Locate every leukocyte (white blood cell).
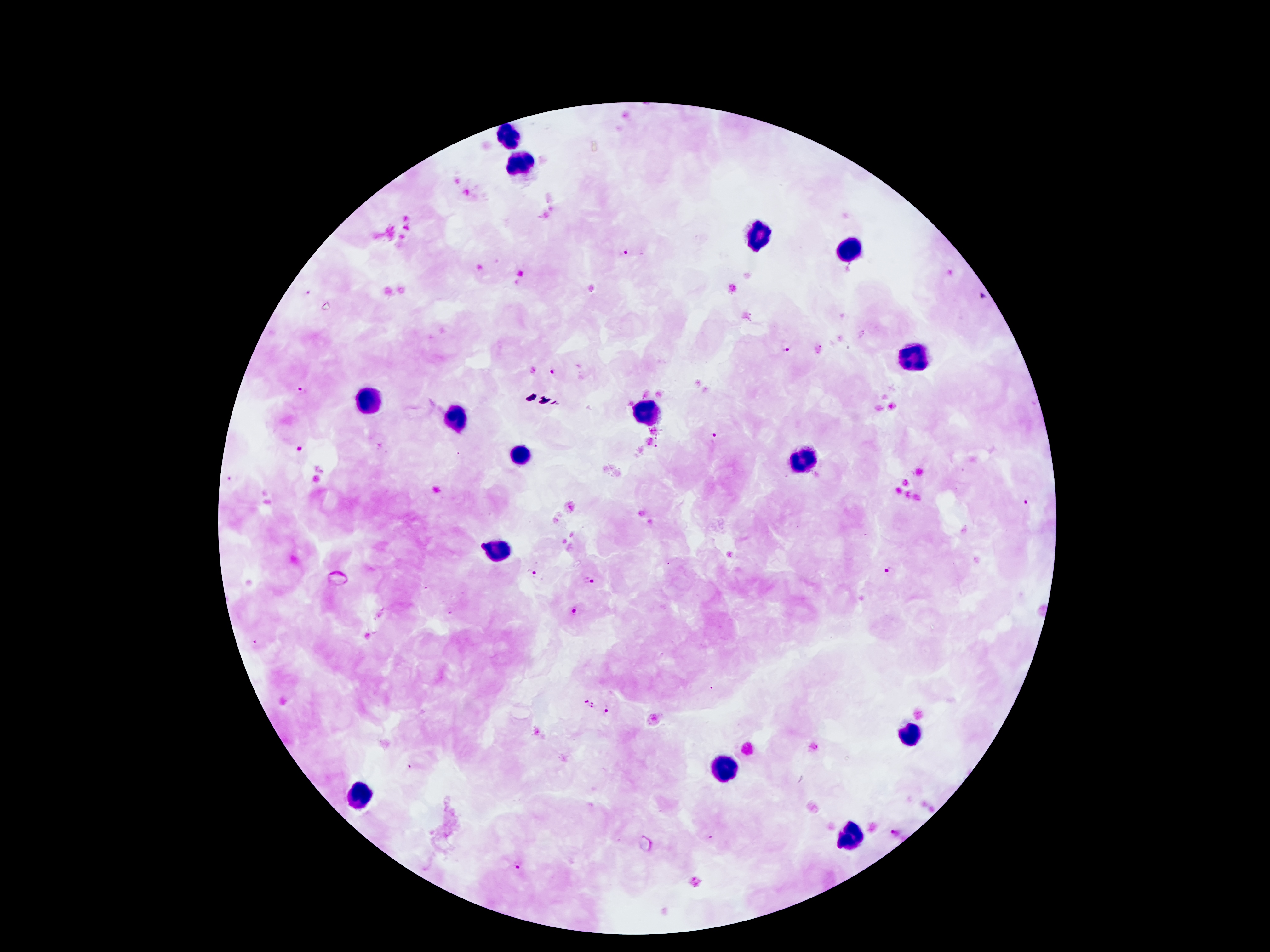
Approximate centers as (x, y) in pixels.
Leukocytes: (507, 137), (519, 162), (761, 235), (850, 248), (916, 357), (371, 401), (648, 410), (453, 416), (519, 455), (800, 462), (500, 550), (907, 734), (724, 768), (362, 792), (853, 835).

{
  "preparation": "thick peripheral-blood smear",
  "field_of_view": "single",
  "patient_malaria_status": "infected with Plasmodium falciparum",
  "capture": "smartphone camera through the microscope eyepiece",
  "image_size": "1270×952 pixels",
  "magnification": "100x",
  "malaria_parasite_locations": "approximate centers as (x, y) in pixels: (625, 251), (308, 292), (983, 297), (788, 348), (554, 372), (301, 389), (715, 435), (299, 448), (232, 477), (1027, 503), (889, 570), (534, 574), (591, 581), (574, 609), (255, 642), (584, 701), (592, 705), (607, 712), (895, 831), (519, 866)",
  "stain": "Giemsa"
}